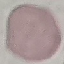
Malaria status: uninfected. Cell patch, automatically extracted from a larger field of view and resized to 64 × 64 pixels. Thin blood film. Photographed with a smartphone camera at the microscope eyepiece. Giemsa-stained preparation.